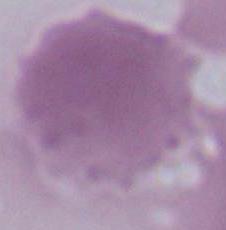

magnification = 1000x
identification = red blood cell
modality = photomicrograph